Evaluate for malaria.
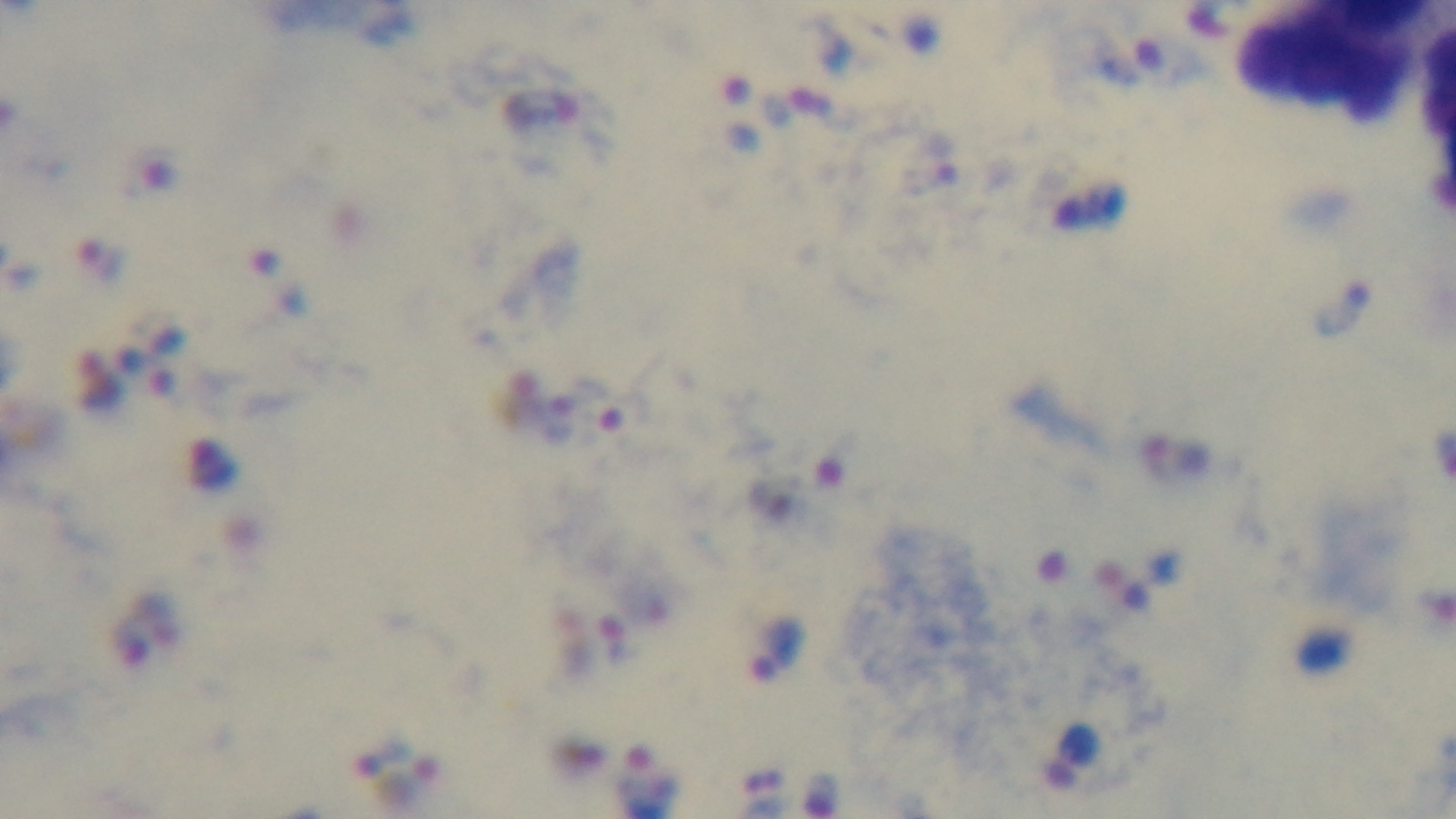
Positive.

Oil-immersion objective, 100x. Giemsa stain. Captured with a mounted 4K digital camera. Preparation: thick. Single field of view. Light microscopy.